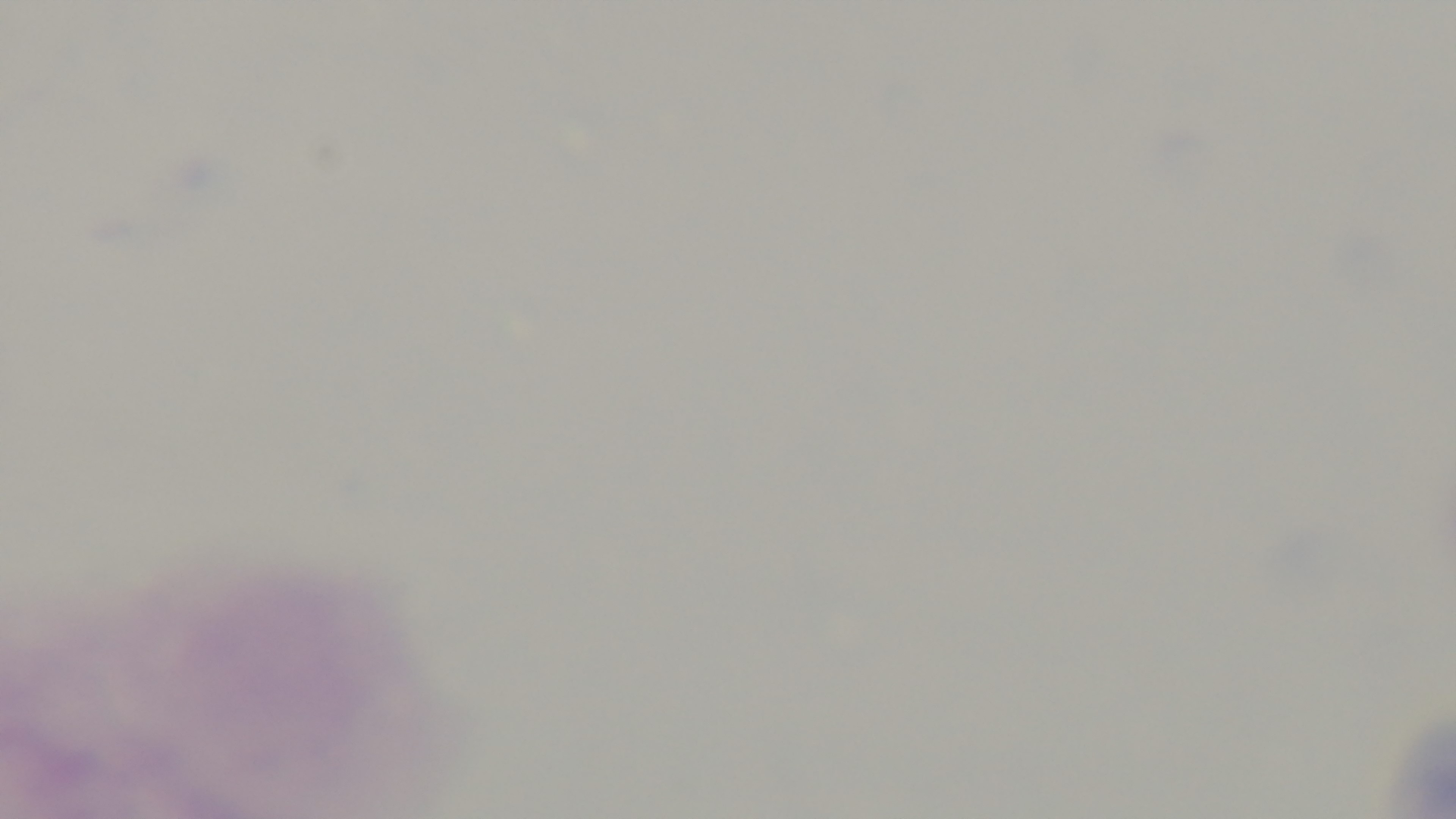
objective = 100x oil immersion
stain = Giemsa
capture = mounted 4K digital camera
preparation = thick blood film
malaria status = negative
field of view = one from the slide
modality = light microscopy